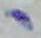
Captured at 1000x magnification. Micrograph. Toxoplasma gondii is seen.